Assess this cell for malaria.
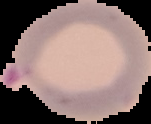
It is parasitized.

Segmented cell region on a black background. From a thin blood smear. Image is 151×124 pixels.